Identify the cell.
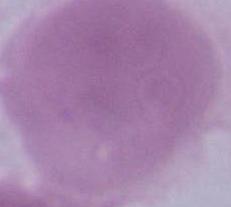

This is an erythrocyte.

Micrograph. 1000x magnification.